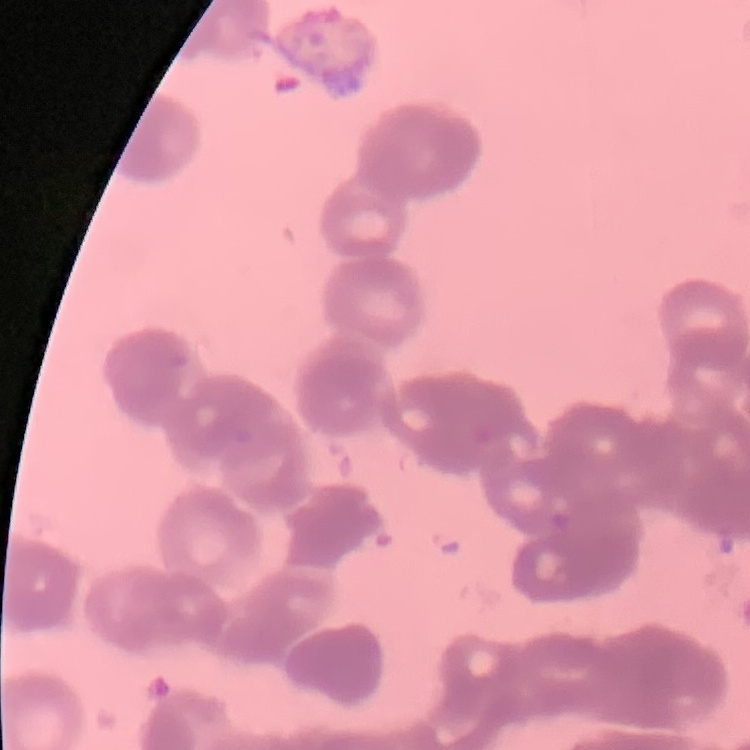

erythrocyte_morphology: rouleaux formation
image_type: square crop of a larger photomicrograph
stain: Field's or Giemsa
preparation: thin blood film